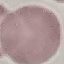

Summary:
  - Malaria status: uninfected
  - Stain: Giemsa
  - Preparation: thin blood film
  - Capture: smartphone camera at the microscope eyepiece
  - Image type: cell patch, automatically extracted from a larger field of view and resized to 64 × 64 pixels